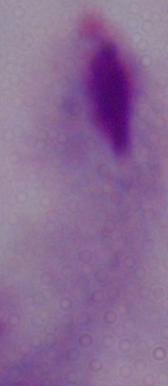

magnification: 1000x
modality: micrograph
identification: trichomonad